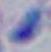
Summary:
  - Identification: Toxoplasma gondii
  - Modality: photomicrograph
  - Magnification: 1000x